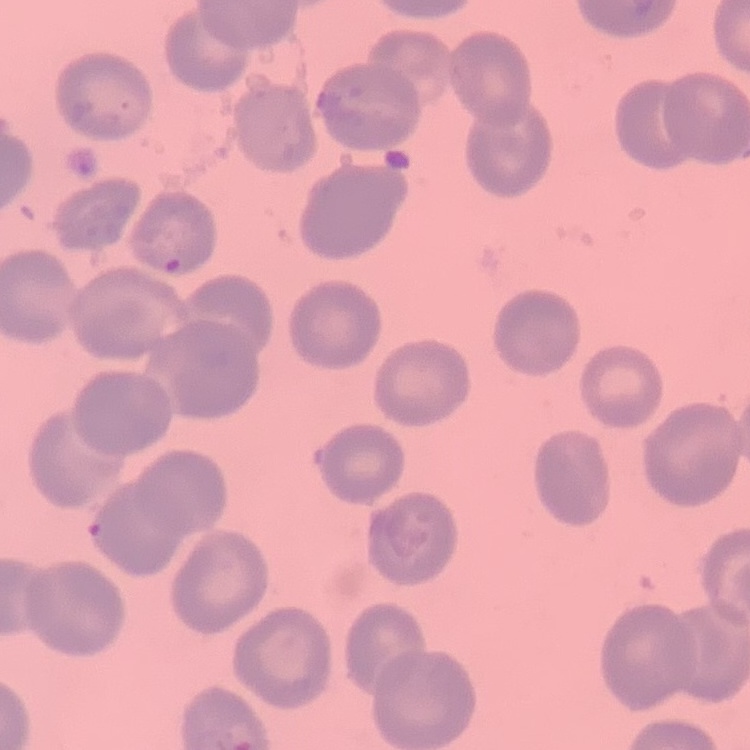

Summary:
  - Erythrocyte morphology: no rouleaux formation
  - Preparation: thin peripheral smear
  - Stain: Field's or Giemsa
  - Image type: square crop of a larger photomicrograph